Classify this cell by malaria status.
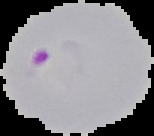

It is parasitized.

{
  "preparation": "thin blood smear",
  "image_type": "cell region segmented out of the field of view; surrounding area masked to black",
  "image_size": "154×136 pixels"
}